Describe the morphology of the red blood cells.
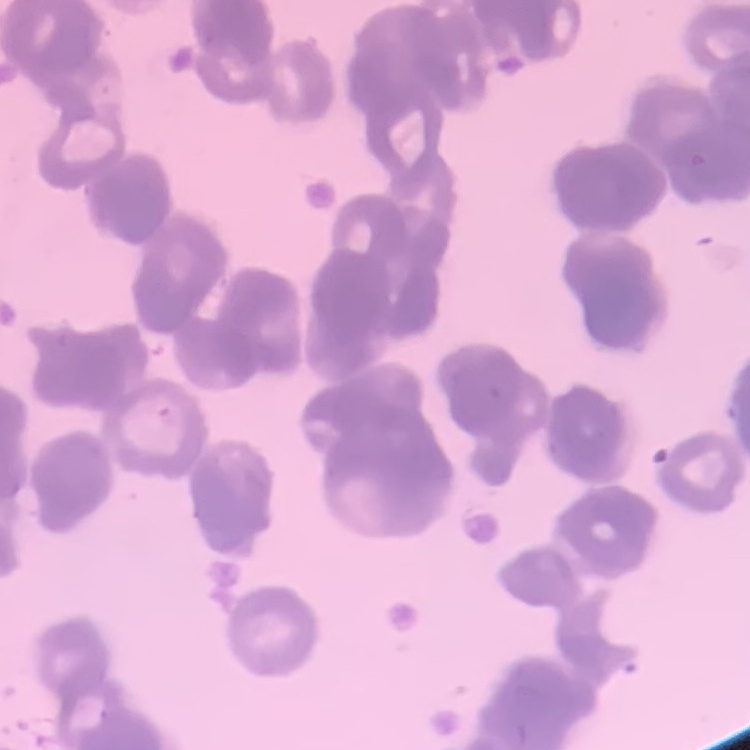
Rouleaux formation.

Stained with either Field's or Giemsa. Square crop of a larger photomicrograph. Thin blood smear.